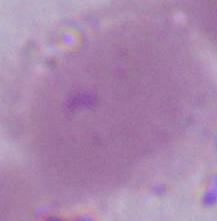

An erythrocyte is shown. Micrograph. Captured at 1000x magnification.